Identify the preparation type.
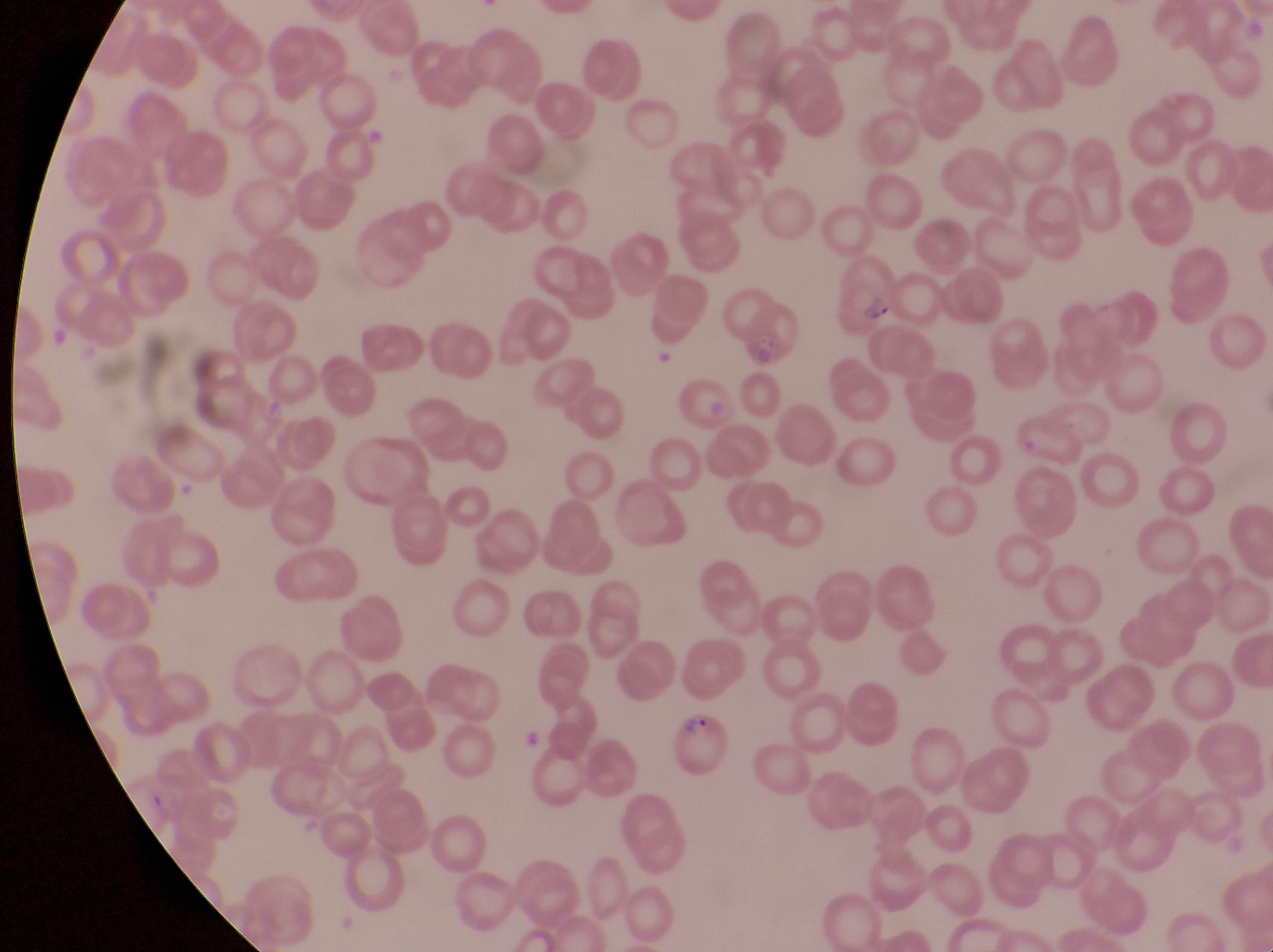

This is a thin smear.

field of view = single
magnification = 1000x
image size = 1273×952 pixels
country = Uganda
parasitised red blood cell locations = approximate bounding boxes as (left, top, right, bottom) in pixels: (828, 264, 906, 331), (739, 306, 800, 367), (674, 712, 734, 786)
capture = smartphone photograph through the eyepiece of an Olympus CX-23 microscope
artifact (platelet-like body, stain precipitate, or debris) locations = approximate bounding boxes as (left, top, right, bottom) in pixels: (523, 725, 542, 748)